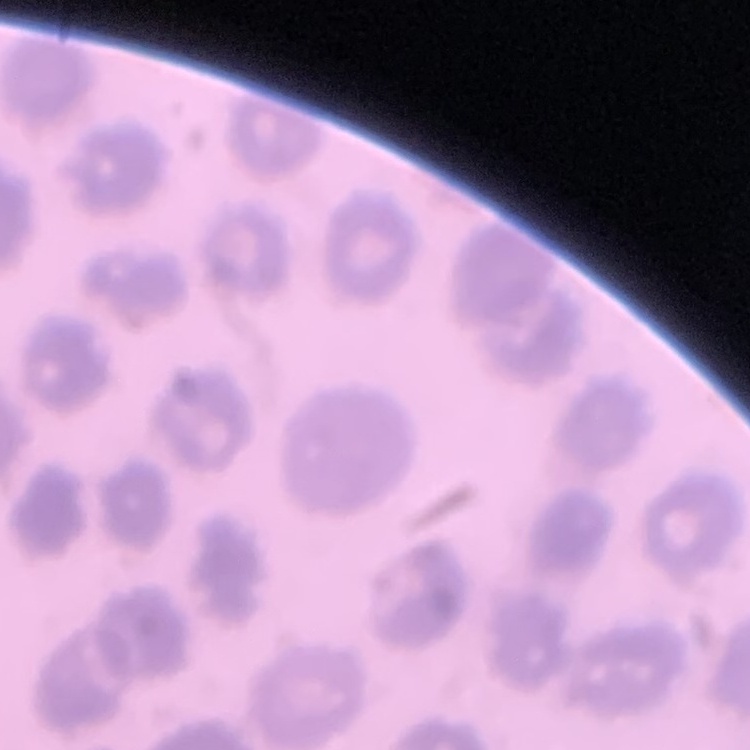 The red blood cells exhibit no rouleaux formation. Field's or Giemsa stain. Square crop of a larger photomicrograph. Thin blood smear.